Assess this cell for malaria.
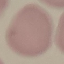

It is uninfected.

Summary:
  - Capture: smartphone through the microscope eyepiece
  - Image type: cell patch, automatically extracted from a larger field of view and resized to 64 × 64 pixels
  - Stain: Giemsa
  - Preparation: thin smear